State which parasite is depicted.
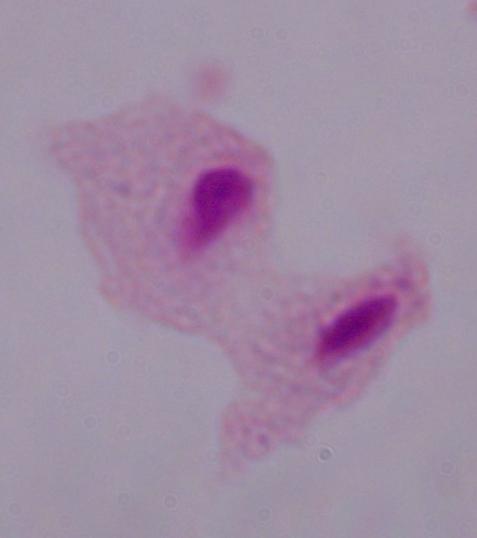
This is a trichomonad.

Summary:
  - Modality: photomicrograph
  - Magnification: 1000x